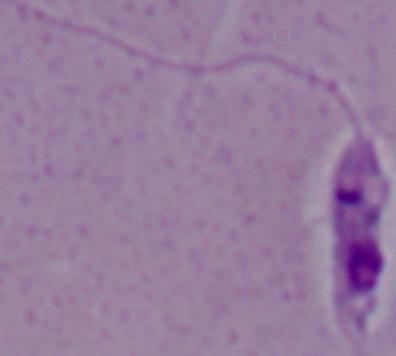
A Leishmania parasite is shown. 1000x magnification. Micrograph.